State which cell type is depicted.
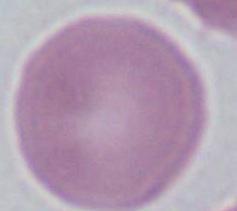
This is an erythrocyte.

Summary:
  - Magnification: 1000x
  - Modality: photomicrograph